Locate and identify every blood parasite.
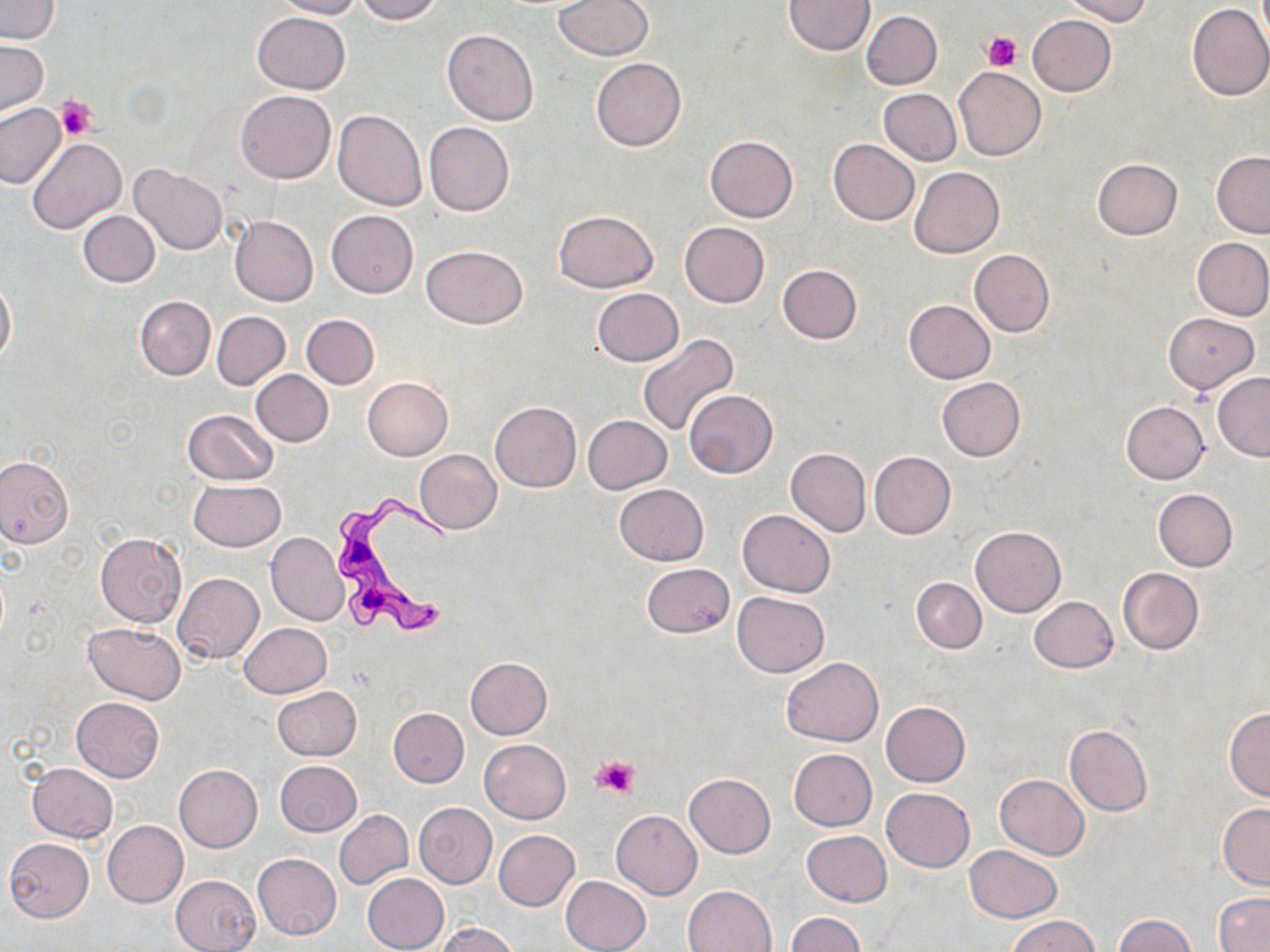
Approximate bounding boxes as (x1,y1)-(x2,y2) corner pairs in pixels.
Trypanosoma brucei: (330,489)-(450,639).
No Plasmodium falciparum, Plasmodium ovale, Plasmodium malariae, Plasmodium vivax, or Babesia divergens observed.

Uninfected red blood cell locations: (275,0)-(362,19), (355,0)-(443,24), (555,0)-(653,60), (1061,0)-(1151,24), (1,1)-(60,43), (784,1)-(876,54), (1186,4)-(1270,102), (871,10)-(948,167), (861,11)-(941,90), (252,12)-(351,94), (1026,14)-(1116,96), (441,28)-(539,125), (0,39)-(49,118), (591,57)-(686,152), (954,66)-(1045,161), (878,89)-(961,166), (234,91)-(335,184), (0,102)-(67,189), (333,110)-(426,210), (424,122)-(514,216), (705,135)-(797,223), (26,137)-(125,234), (828,139)-(920,225), (1211,152)-(1270,239), (1092,157)-(1184,240), (129,164)-(228,255), (909,167)-(1004,258), (325,210)-(418,298), (554,210)-(658,292), (77,211)-(160,287), (230,214)-(318,305), (679,222)-(770,308), (1193,236)-(1270,320), (422,244)-(527,328), (970,249)-(1054,337), (778,265)-(862,344), (0,277)-(16,366), (593,288)-(683,367), (135,295)-(216,380), (903,300)-(995,384), (211,311)-(290,390), (1163,312)-(1260,394), (301,314)-(379,390), (637,334)-(740,438), (250,370)-(333,446), (1212,373)-(1270,462), (363,377)-(453,459), (936,377)-(1025,461), (684,390)-(778,477), (1120,400)-(1209,483), (490,401)-(582,492), (182,409)-(278,486), (582,415)-(672,494), (786,448)-(870,536), (415,449)-(501,533), (869,451)-(955,540), (0,455)-(73,548), (188,480)-(286,551), (615,484)-(709,565), (1152,489)-(1237,571), (736,509)-(835,596), (971,526)-(1066,616), (95,532)-(186,627), (265,532)-(347,625), (641,563)-(735,638), (1117,567)-(1204,655), (172,572)-(263,663), (911,577)-(985,654), (732,592)-(829,677), (1028,596)-(1118,672), (83,622)-(186,703), (239,622)-(332,698), (465,657)-(552,740), (781,657)-(883,747), (272,687)-(361,761), (71,696)-(164,783), (881,700)-(970,786), (388,707)-(469,787), (1226,707)-(1270,800), (1064,725)-(1152,816), (480,739)-(571,824), (788,748)-(877,830), (275,759)-(362,836), (28,763)-(118,843), (174,763)-(262,852), (684,773)-(776,857), (995,773)-(1089,860), (880,786)-(975,872), (413,803)-(498,888), (1218,804)-(1270,891), (610,809)-(701,900), (334,810)-(413,889), (103,820)-(188,907), (494,830)-(579,911), (801,830)-(890,908), (4,837)-(94,922), (963,845)-(1062,923), (253,853)-(342,940), (362,873)-(449,952), (171,874)-(261,952), (561,875)-(651,952), (684,884)-(776,951), (1213,891)-(1270,952), (787,912)-(864,952), (1114,914)-(1196,951), (1008,916)-(1100,952), (435,922)-(520,952). Platelet locations: (983,32)-(1022,72), (54,95)-(96,140), (593,754)-(641,799). Slide-level diagnosis: Trypanosoma brucei. Thin blood film. Image is 1270×952 pixels. 1000x magnification. Optical microscopy. Single field of view. May-Grünwald-Giemsa stain.